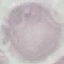

Summary:
  - Result: no malaria parasites detected
  - Image type: automatically extracted cell patch, resized to 64 × 64 pixels
  - Capture: smartphone camera at the microscope eyepiece
  - Stain: Giemsa
  - Preparation: thin blood film